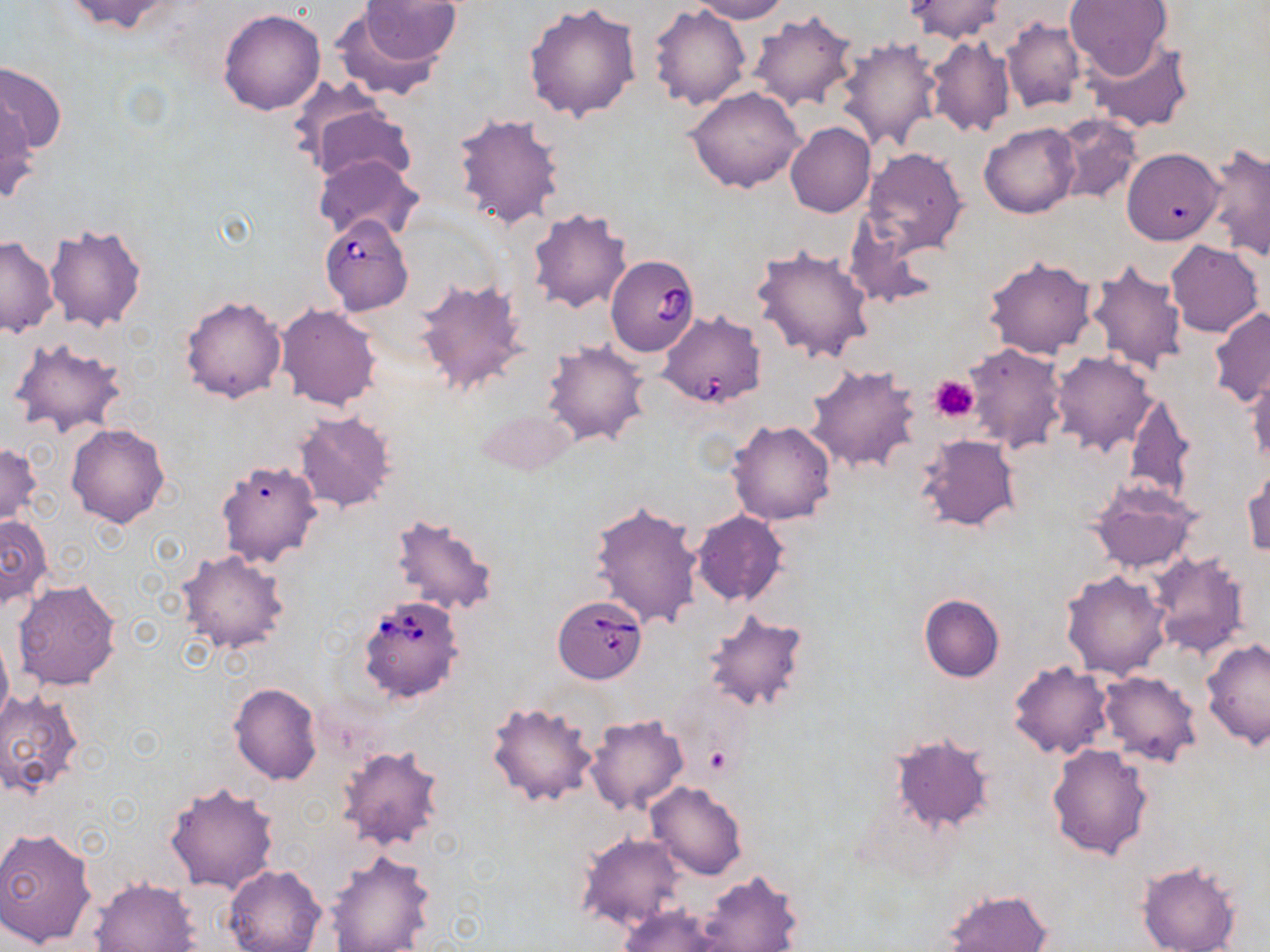
slide_level_diagnosis: Babesia divergens
magnification: 1000x
platelet_locations: 'approximate bounding boxes as (x1, y1, x2, y2) in pixels: (929, 376, 978, 422), (703, 745, 733, 775)'
preparation: thin blood smear
image_size: 1270×952 pixels
modality: optical microscopy
uninfected_red_blood_cell_locations: 'approximate bounding boxes as (x1, y1, x2, y2) in pixels: (61, 0, 188, 36), (360, 0, 462, 66), (685, 0, 789, 23), (904, 0, 1010, 44), (1063, 0, 1173, 78), (524, 2, 641, 121), (650, 4, 751, 110), (217, 8, 325, 115), (329, 9, 447, 103), (747, 11, 859, 111), (1000, 19, 1085, 114), (925, 35, 1017, 139), (833, 36, 943, 152), (1084, 36, 1191, 134), (0, 62, 65, 157), (686, 86, 805, 193), (0, 95, 38, 205), (302, 98, 413, 184), (451, 111, 565, 231), (1051, 114, 1141, 204), (979, 121, 1079, 218), (785, 122, 875, 218), (1202, 143, 1270, 259), (861, 146, 969, 258), (1122, 146, 1224, 245), (314, 155, 422, 243), (527, 207, 633, 313), (839, 213, 939, 309), (44, 221, 147, 333), (0, 235, 58, 337), (1165, 241, 1264, 338), (752, 244, 875, 364), (983, 256, 1098, 360), (1085, 259, 1188, 375), (413, 276, 529, 398), (180, 294, 287, 402), (275, 304, 381, 410), (1209, 307, 1270, 408), (7, 336, 131, 438), (541, 339, 649, 446), (961, 342, 1068, 454), (1050, 351, 1155, 454), (806, 363, 923, 474), (1246, 367, 1270, 467), (1123, 393, 1194, 503), (479, 405, 576, 477), (294, 410, 398, 513), (726, 420, 837, 525), (67, 423, 170, 528), (917, 434, 1020, 532), (0, 442, 41, 526), (216, 459, 322, 567), (1243, 464, 1270, 560), (1090, 481, 1200, 574), (589, 501, 702, 630), (691, 511, 789, 606), (390, 512, 499, 617), (1, 513, 52, 608), (176, 549, 290, 655), (1148, 552, 1250, 657), (1061, 570, 1171, 680), (12, 579, 122, 691), (919, 594, 1004, 683), (700, 607, 810, 713), (0, 630, 12, 733), (1201, 639, 1269, 749), (1008, 661, 1113, 759), (1097, 671, 1202, 768), (229, 683, 323, 785), (0, 688, 85, 800), (486, 699, 601, 807), (584, 714, 689, 815), (890, 732, 995, 833), (336, 743, 446, 852), (1046, 743, 1153, 859), (164, 782, 279, 894), (645, 782, 746, 880), (0, 826, 98, 948), (578, 833, 686, 932), (322, 850, 435, 952), (1136, 860, 1243, 952), (226, 865, 327, 952), (697, 870, 803, 951), (91, 878, 200, 951), (940, 889, 1053, 952), (616, 905, 730, 951)'
babesia_divergens_infected_red_blood_cell_locations: 'approximate bounding boxes as (x1, y1, x2, y2) in pixels: (320, 215, 414, 317), (604, 255, 699, 356), (657, 309, 765, 408), (357, 594, 466, 702), (554, 600, 645, 682)'
field_of_view: single
stain: May-Grünwald-Giemsa